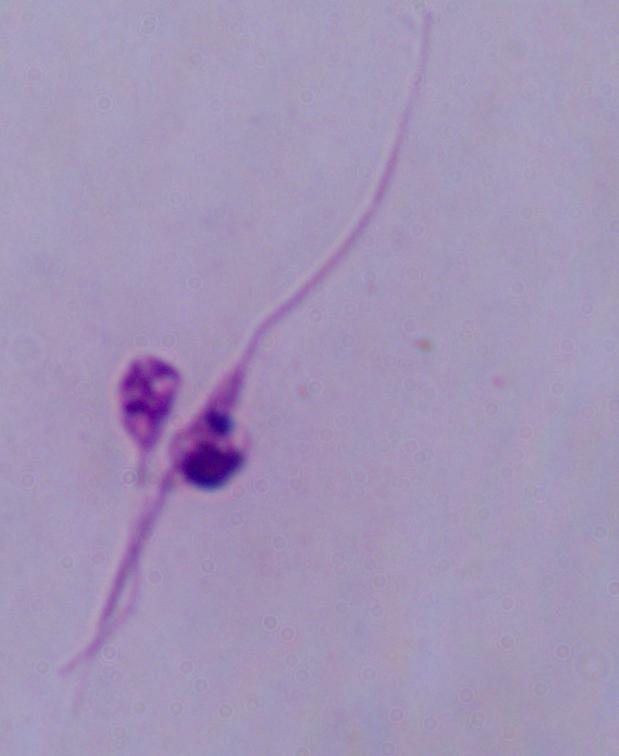

modality: micrograph
identification: Leishmania
magnification: 1000x